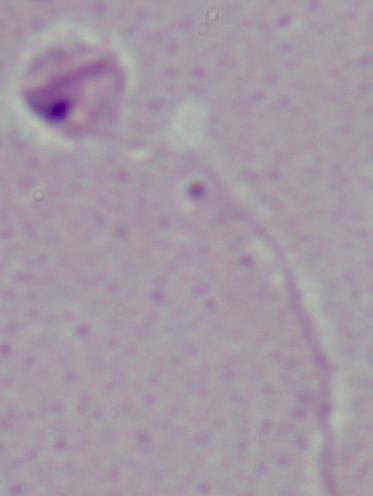 Photomicrograph. 1000x magnification. A Leishmania parasite is seen.